Classify this cell by malaria status.
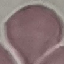

Uninfected.

Cell patch, automatically extracted from a larger field of view and resized to 64 × 64 pixels. Photographed with a smartphone camera at the microscope eyepiece. Giemsa stain. Thin smear of blood.